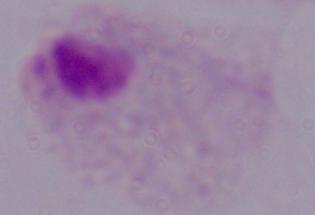
Summary:
  - Modality: photomicrograph
  - Magnification: 1000x
  - Identification: trichomonad